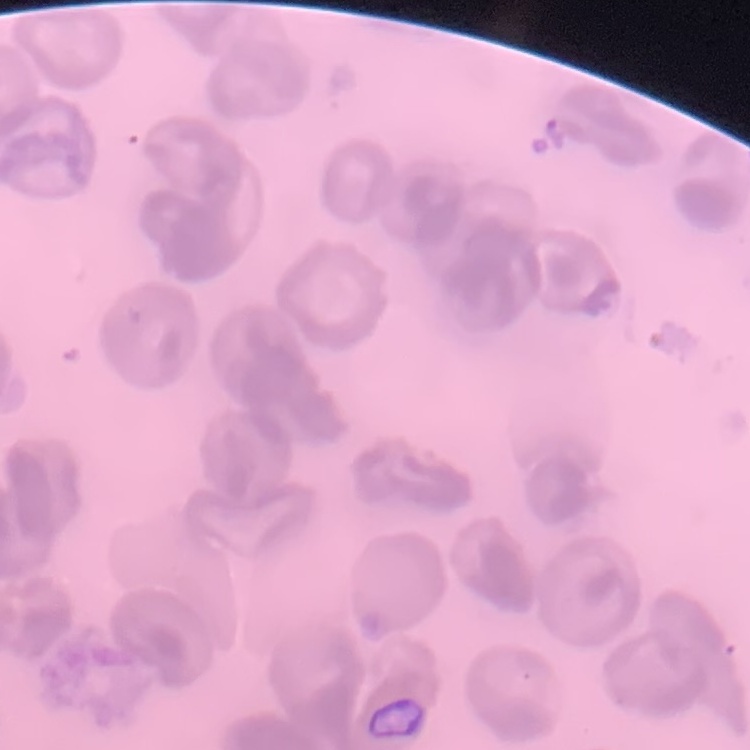
Summary:
  - Erythrocyte morphology: no rouleaux formation
  - Stain: Field's or Giemsa
  - Image type: one tile cut from a larger photomicrograph
  - Preparation: thin blood smear